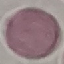

Summary:
  - Result: no malaria parasites seen
  - Capture: smartphone through the microscope eyepiece
  - Stain: Giemsa
  - Preparation: thin blood film
  - Image type: automatically extracted cell patch, resized to 64 × 64 pixels